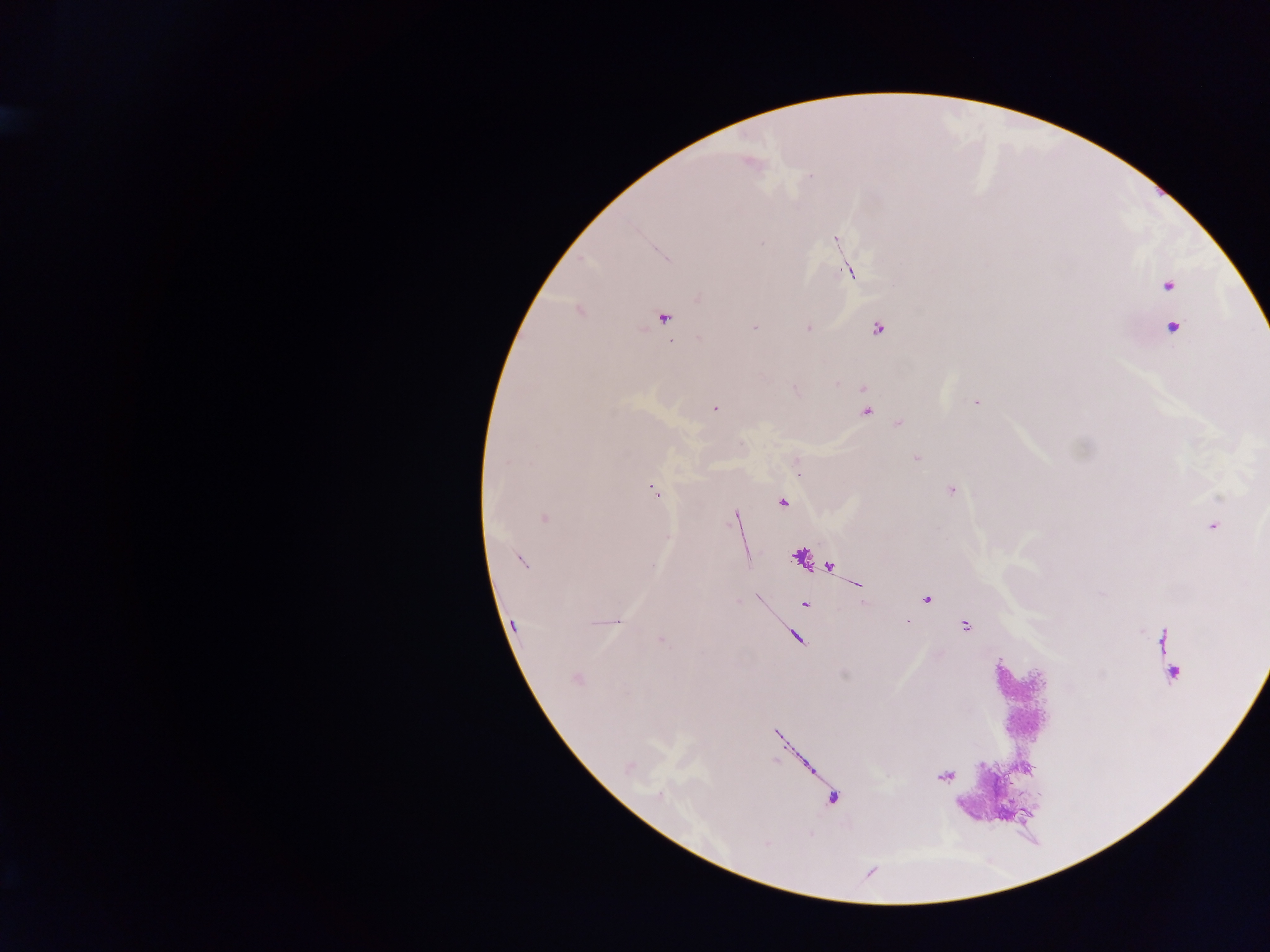

field of view = single
country = Ghana
image size = 1270×952 pixels
capture = mobile-phone photograph through a microscope
malaria parasite locations = approximate centers as (x, y) in pixels: (751, 163), (810, 176), (835, 239), (762, 244), (666, 259), (848, 271), (1168, 286), (698, 298), (664, 318), (755, 326), (807, 328), (1172, 328), (878, 329), (699, 338), (977, 402), (715, 409), (866, 412), (899, 424), (917, 458), (506, 462), (798, 468), (951, 490), (654, 492), (782, 502), (544, 518), (735, 518), (1212, 526), (521, 560), (653, 566), (926, 599), (805, 605), (617, 621), (513, 624), (965, 627), (661, 640), (576, 679), (767, 843)
preparation = thick blood smear